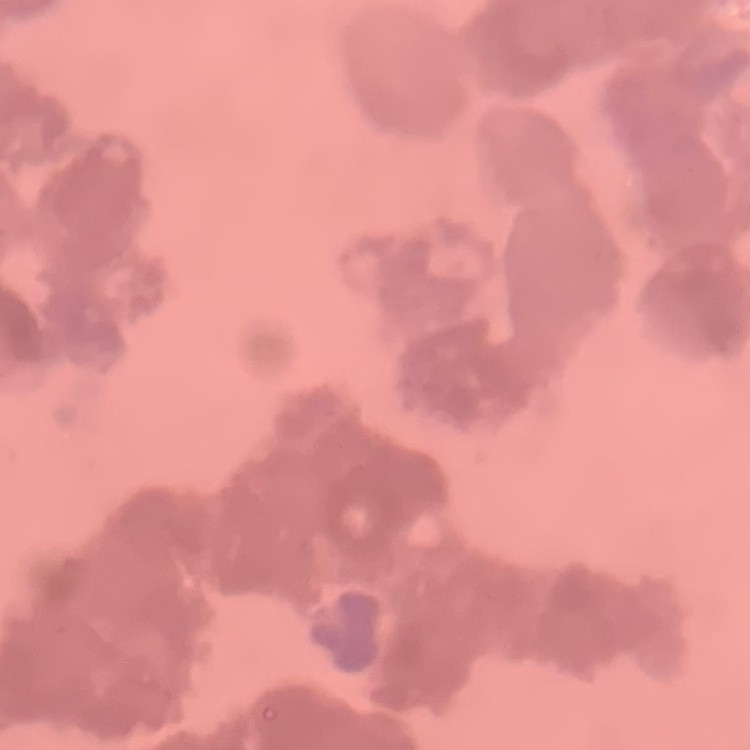 The red blood cells exhibit rouleaux formation. Square crop of a larger photomicrograph. Thin blood smear. Stained with either Field's or Giemsa.